Name the blood parasite species.
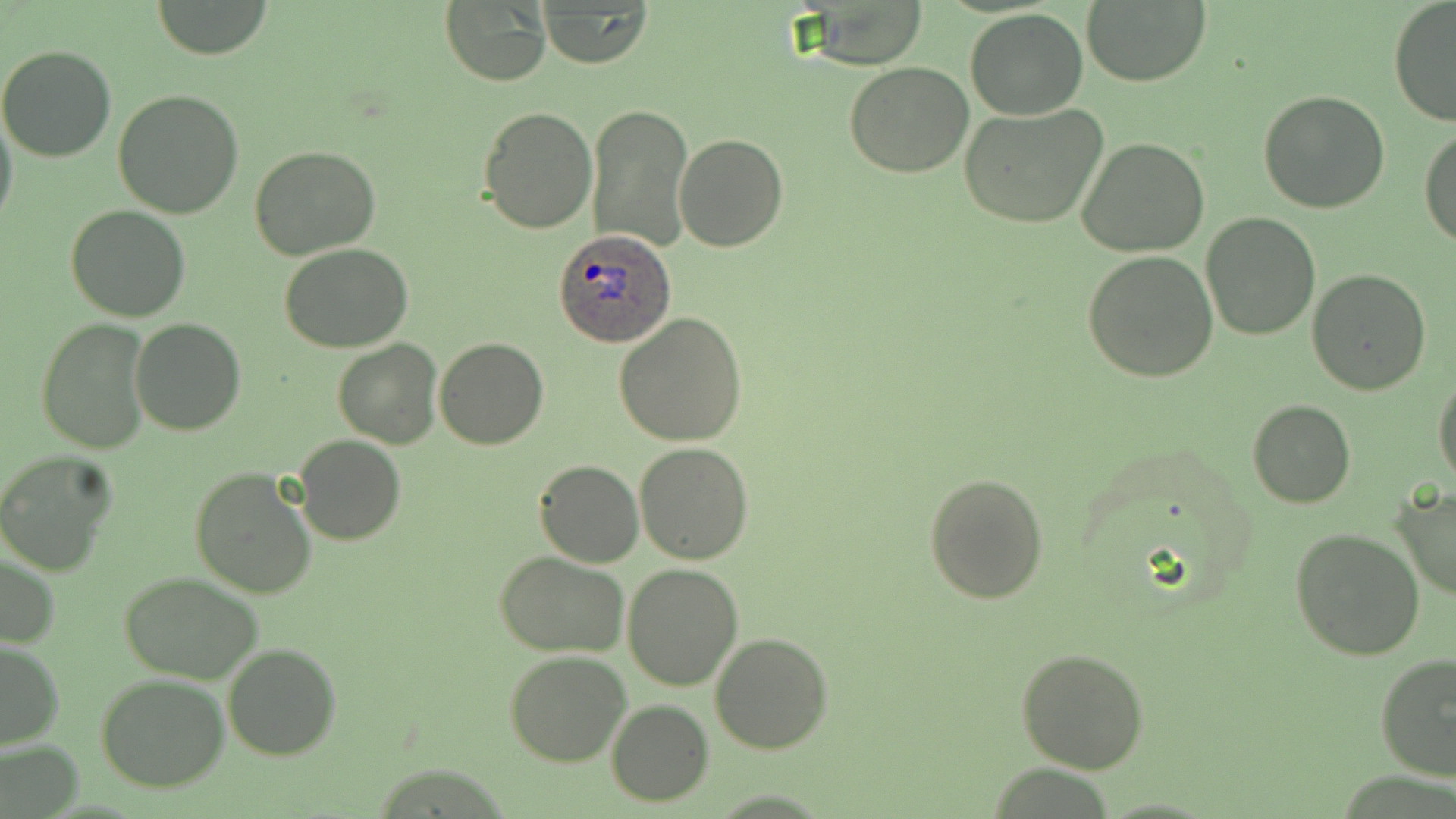
Plasmodium ovale.

Summary:
  - Coordinate format: approximate bounding boxes as named x1/y1/x2/y2 corners in pixels
  - Plasmodium ovale-infected red blood cell locations: (x1=556, y1=229, x2=676, y2=349)
  - Uninfected red blood cell locations: (x1=147, y1=1, x2=274, y2=59), (x1=1081, y1=1, x2=1210, y2=86), (x1=1387, y1=1, x2=1456, y2=127), (x1=438, y1=2, x2=551, y2=86), (x1=537, y1=3, x2=652, y2=68), (x1=965, y1=9, x2=1088, y2=119), (x1=0, y1=45, x2=117, y2=163), (x1=844, y1=61, x2=975, y2=177), (x1=111, y1=89, x2=244, y2=219), (x1=1258, y1=89, x2=1390, y2=212), (x1=586, y1=102, x2=693, y2=252), (x1=958, y1=103, x2=1109, y2=230), (x1=479, y1=104, x2=598, y2=233), (x1=0, y1=108, x2=17, y2=235), (x1=1420, y1=125, x2=1456, y2=247), (x1=674, y1=132, x2=788, y2=252), (x1=1075, y1=136, x2=1209, y2=257), (x1=249, y1=145, x2=381, y2=260), (x1=64, y1=204, x2=191, y2=322), (x1=1200, y1=213, x2=1322, y2=340), (x1=278, y1=243, x2=413, y2=352), (x1=1082, y1=251, x2=1219, y2=382), (x1=1307, y1=269, x2=1433, y2=395), (x1=614, y1=313, x2=747, y2=447), (x1=37, y1=319, x2=151, y2=453), (x1=131, y1=320, x2=245, y2=437), (x1=435, y1=337, x2=548, y2=450), (x1=332, y1=339, x2=444, y2=450), (x1=1433, y1=371, x2=1456, y2=487), (x1=1246, y1=399, x2=1356, y2=508), (x1=294, y1=435, x2=405, y2=545), (x1=633, y1=442, x2=754, y2=564), (x1=0, y1=451, x2=117, y2=576), (x1=535, y1=460, x2=644, y2=568), (x1=189, y1=467, x2=317, y2=599), (x1=923, y1=471, x2=1049, y2=604), (x1=1391, y1=486, x2=1456, y2=603), (x1=1291, y1=528, x2=1426, y2=663), (x1=496, y1=551, x2=627, y2=657), (x1=1, y1=552, x2=60, y2=650), (x1=623, y1=561, x2=744, y2=691), (x1=118, y1=570, x2=267, y2=684), (x1=710, y1=632, x2=833, y2=753), (x1=0, y1=640, x2=64, y2=748), (x1=223, y1=643, x2=341, y2=762), (x1=1017, y1=647, x2=1149, y2=774), (x1=505, y1=650, x2=632, y2=767), (x1=1376, y1=653, x2=1456, y2=782), (x1=97, y1=673, x2=230, y2=791), (x1=607, y1=699, x2=713, y2=805), (x1=1, y1=741, x2=83, y2=817)
  - Image size: 1456×819 pixels
  - Preparation: thin blood film
  - Field of view: one of a larger specimen
  - Stain: May-Grünwald-Giemsa
  - Magnification: 1000x
  - Modality: light microscopy